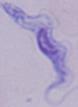

Micrograph. A trypanosome is shown. Captured at 1000x magnification.